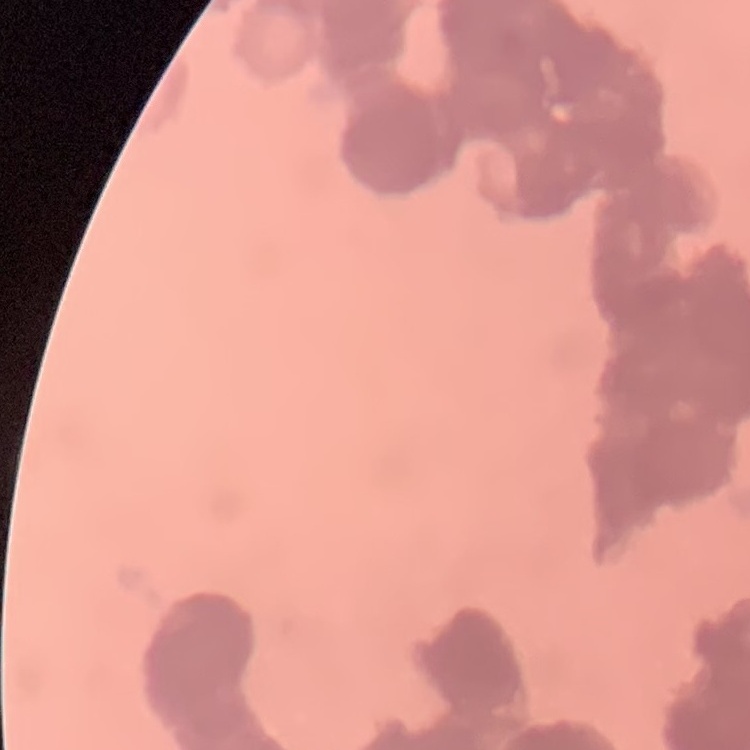

The erythrocytes show rouleaux formation. Square crop of a larger photomicrograph. Field's or Giemsa stain. Thin blood film.